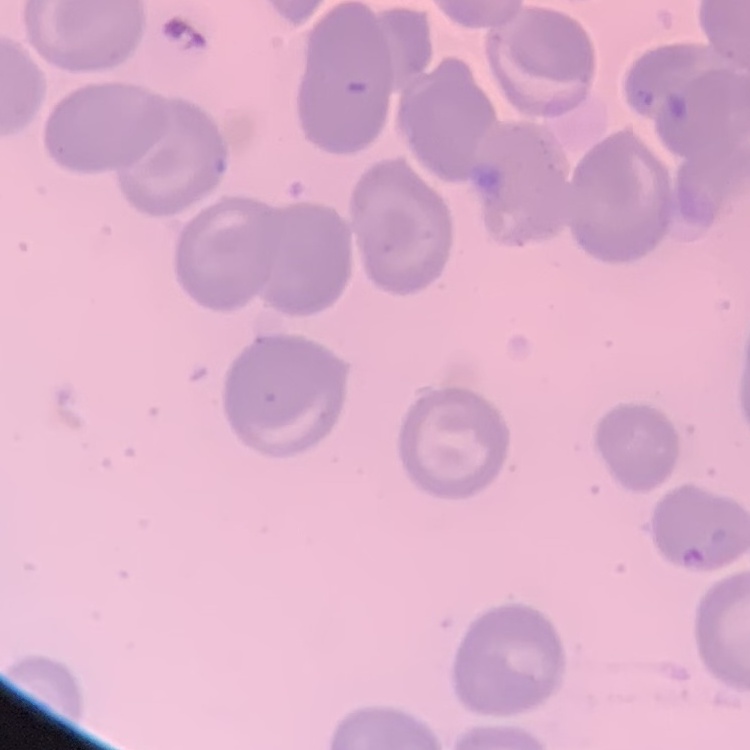
Summary:
  - Erythrocyte morphology: no rouleaux formation
  - Stain: Field's or Giemsa
  - Preparation: thin peripheral smear
  - Image type: one tile cut from a larger photomicrograph